Locate the cells, classifying each as a parasitized RBC, an uninfected RBC, or a WBC.
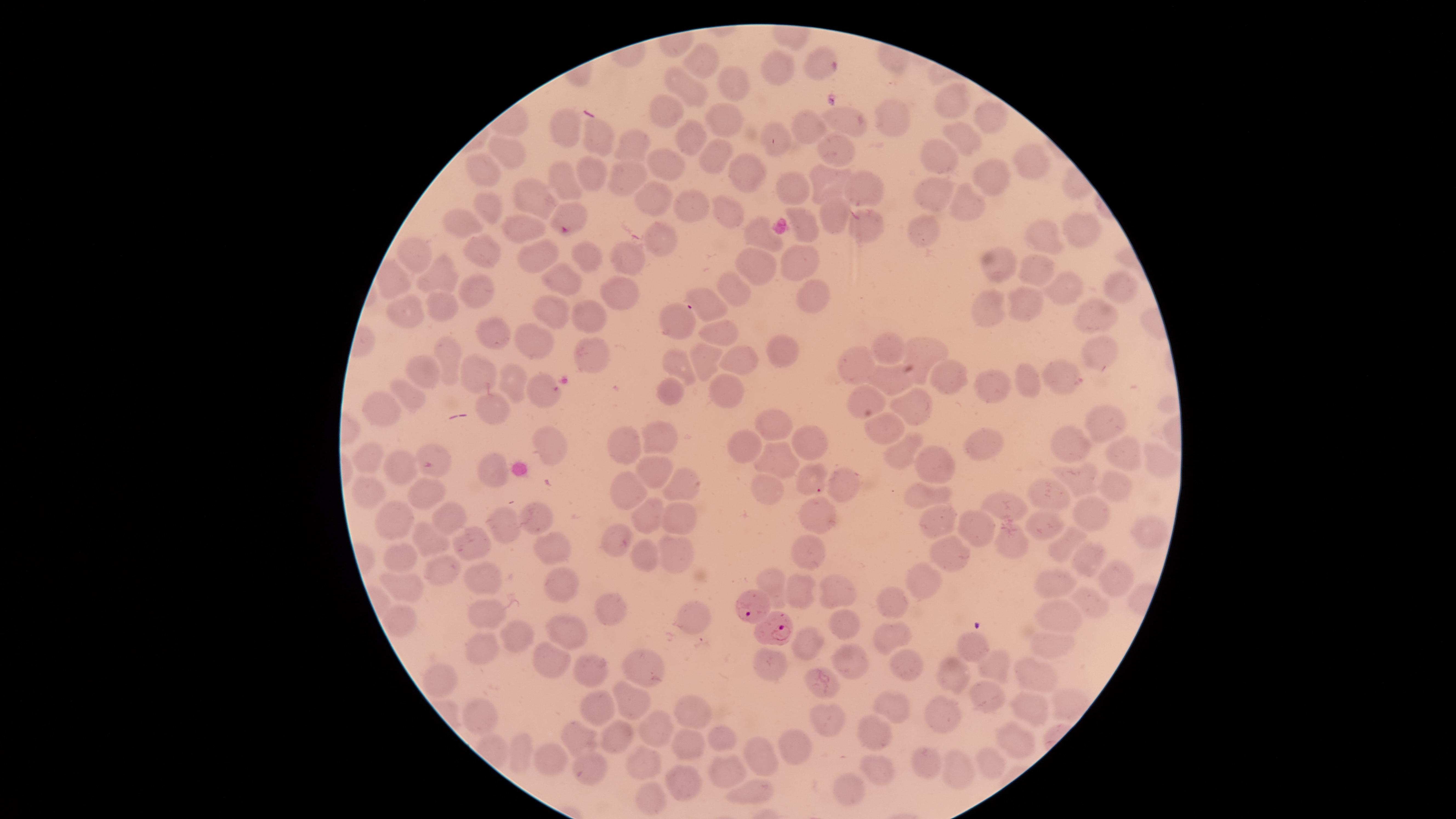

Approximate marker points as {x, y} in pixels.
Parasitized RBCs: {569, 219}, {752, 608}, {776, 631}.
Uninfected RBCs: {703, 60}, {816, 60}, {774, 70}, {728, 78}, {686, 82}, {951, 98}, {670, 112}, {986, 113}, {886, 115}, {722, 118}, {845, 119}, {812, 123}, {561, 125}, {958, 132}, {595, 137}, {691, 137}, {779, 142}, {630, 143}, {837, 147}, {505, 151}, {714, 157}, {939, 159}, {669, 165}, {748, 168}, {1034, 168}, {486, 170}, {585, 173}, {989, 174}, {622, 178}, {565, 182}, {828, 182}, {868, 186}, {791, 189}, {936, 189}, {656, 196}, {963, 199}, {532, 201}, {688, 204}, {489, 205}, {727, 208}, {829, 211}, {465, 222}, {866, 223}, {802, 225}, {1080, 226}, {522, 229}, {752, 230}, {927, 230}, {662, 241}, {1045, 241}, {412, 253}, {484, 254}, {541, 255}, {584, 255}, {627, 256}, {796, 258}, {759, 264}, {996, 266}, {1033, 266}, {444, 275}, {565, 280}, {1122, 283}, {1061, 284}, {736, 286}, {476, 287}, {617, 291}, {811, 294}, {1026, 303}, {711, 304}, {447, 306}, {987, 307}, {553, 312}, {405, 314}, {1091, 314}, {589, 315}, {673, 320}, {494, 327}, {716, 330}, {534, 343}, {887, 344}, {926, 348}, {1100, 348}, {785, 349}, {592, 353}, {739, 357}, {451, 360}, {678, 360}, {707, 360}, {863, 364}, {1057, 369}, {429, 370}, {949, 371}, {480, 373}, {889, 374}, {1027, 380}, {509, 382}, {993, 385}, {725, 387}, {541, 392}, {411, 393}, {863, 395}, {670, 396}, {490, 405}, {914, 407}, {384, 408}, {1108, 421}, {772, 422}, {887, 426}, {547, 437}, {805, 437}, {659, 438}, {743, 441}, {984, 441}, {1069, 442}, {621, 443}, {905, 450}, {1129, 453}, {935, 456}, {371, 459}, {778, 459}, {1160, 461}, {399, 468}, {649, 469}, {495, 473}, {807, 475}, {844, 477}, {1080, 478}, {681, 481}, {1119, 485}, {625, 486}, {364, 487}, {767, 488}, {426, 492}, {923, 494}, {1056, 499}, {1001, 508}, {646, 512}, {1086, 512}, {816, 513}, {536, 515}, {452, 516}, {388, 520}, {504, 522}, {933, 522}, {684, 523}, {1044, 525}, {975, 530}, {1152, 531}, {619, 537}, {465, 538}, {427, 539}, {1011, 543}, {1060, 546}, {546, 551}, {676, 552}, {1082, 553}, {802, 554}, {642, 556}, {400, 558}, {946, 558}, {444, 570}, {1108, 574}, {481, 576}, {918, 578}, {770, 579}, {556, 580}, {1057, 584}, {408, 586}, {841, 588}, {800, 590}, {890, 600}, {1093, 602}, {483, 607}, {617, 611}, {1056, 611}, {396, 620}, {692, 622}, {846, 626}, {568, 627}, {891, 631}, {511, 634}, {807, 643}, {1052, 646}, {968, 648}, {484, 651}, {846, 656}, {548, 664}, {643, 664}, {900, 665}, {993, 666}, {770, 668}, {590, 670}, {955, 671}, {436, 677}, {1032, 677}, {825, 687}, {630, 697}, {984, 698}, {891, 704}, {1031, 705}, {590, 707}, {690, 712}, {941, 713}, {481, 715}, {827, 718}, {658, 726}, {871, 732}, {577, 734}, {611, 735}, {1011, 736}, {722, 738}, {684, 740}, {787, 746}, {516, 752}, {756, 752}, {552, 760}, {990, 763}, {590, 765}, {640, 765}, {929, 765}, {876, 767}, {957, 769}, {722, 772}, {685, 778}, {845, 791}, {754, 792}, {651, 796}.
No WBCs identified.

Summary:
  - Image size: 1456×819 pixels
  - Stain: Giemsa
  - Visible region: circular
  - Species: Plasmodium falciparum
  - Field of view: single
  - Preparation: thin blood film
  - Capture: smartphone photograph through the microscope eyepiece